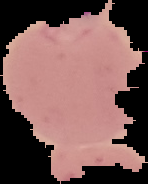
Summary:
  - Preparation: thin blood film
  - Image size: 148×184 pixels
  - Result: Plasmodium parasites identified
  - Image type: segmented cell region with the area outside set to black